Give the extent of all Plasmodium ovale-infected red blood cells.
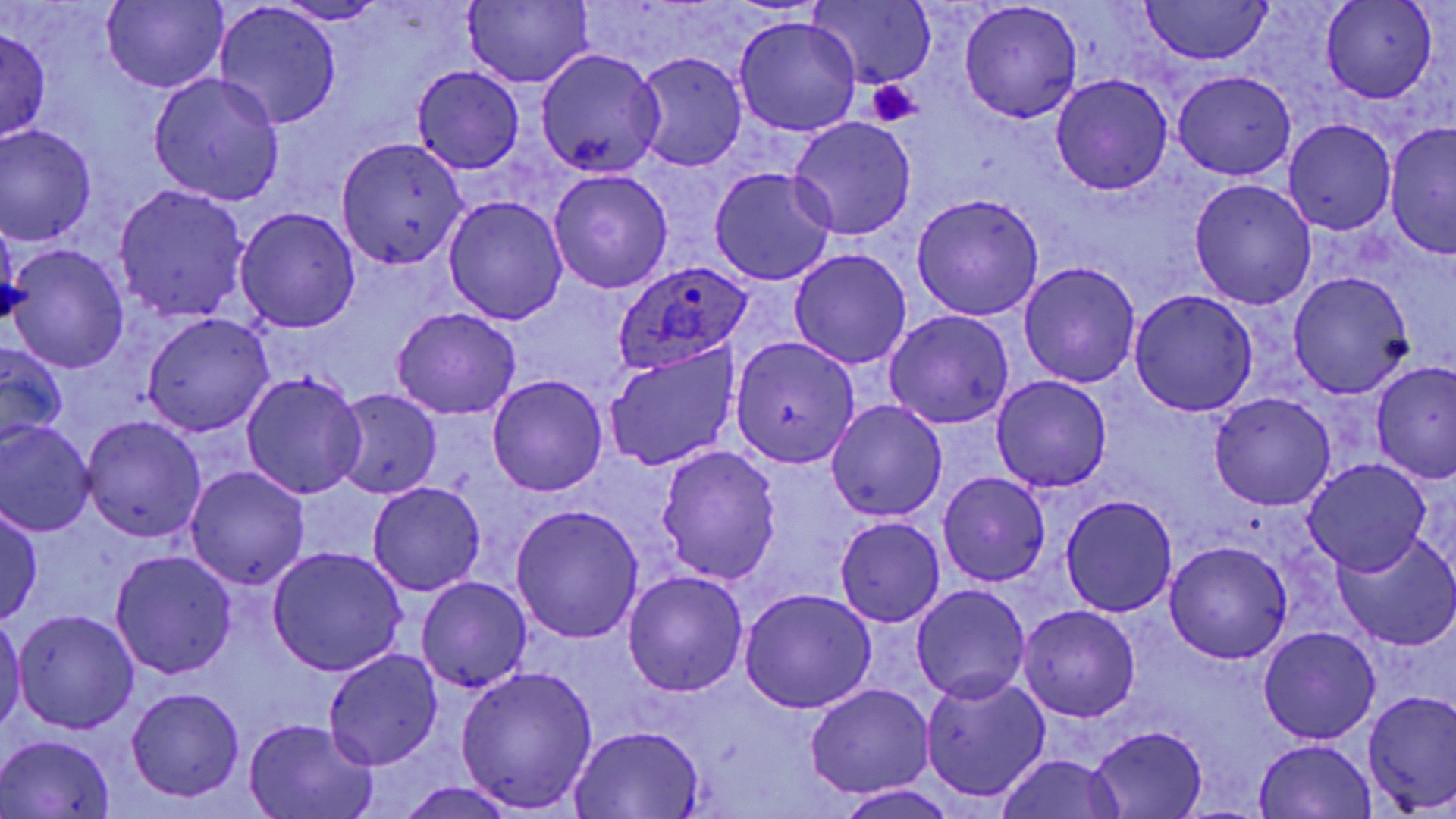
Approximate bounding boxes as [x1, y1, x2, y2] in pixels.
Plasmodium ovale-infected red blood cells: [613, 260, 755, 373].

Platelet locations: [866, 78, 924, 126]. Uninfected red blood cell locations: [805, 0, 936, 90], [1321, 0, 1437, 103], [102, 2, 227, 92], [278, 2, 390, 24], [463, 2, 593, 87], [1138, 2, 1273, 64], [216, 3, 342, 130], [959, 3, 1083, 122], [733, 15, 862, 138], [0, 29, 51, 142], [535, 48, 665, 176], [632, 51, 748, 173], [413, 65, 524, 173], [1173, 69, 1295, 178], [148, 72, 285, 205], [1051, 73, 1173, 195], [788, 117, 917, 241], [1283, 119, 1396, 235], [1385, 122, 1456, 256], [0, 125, 96, 245], [336, 136, 468, 268], [708, 166, 836, 287], [547, 170, 674, 294], [1188, 179, 1317, 309], [114, 185, 250, 324], [912, 193, 1045, 322], [443, 195, 568, 325], [234, 207, 361, 334], [0, 213, 25, 332], [4, 243, 129, 372], [789, 248, 912, 369], [1018, 261, 1141, 388], [1287, 271, 1414, 399], [1129, 289, 1259, 414], [391, 307, 521, 420], [884, 309, 1015, 430], [142, 313, 274, 436], [732, 335, 860, 468], [0, 340, 68, 449], [603, 344, 740, 471], [1371, 360, 1455, 486], [241, 371, 366, 499], [489, 375, 607, 495], [991, 375, 1112, 494], [332, 390, 442, 500], [1210, 392, 1335, 510], [825, 399, 948, 522], [80, 415, 208, 543], [0, 420, 96, 536], [655, 445, 782, 586], [1303, 459, 1432, 577], [186, 465, 310, 591], [937, 471, 1051, 587], [368, 481, 486, 596], [1061, 494, 1178, 616], [0, 504, 44, 624], [510, 504, 643, 641], [311, 507, 461, 640], [834, 515, 946, 627], [1053, 529, 1171, 684], [1331, 530, 1456, 652], [1164, 539, 1293, 663], [267, 547, 407, 676], [109, 552, 237, 678], [622, 571, 748, 697], [416, 577, 531, 693], [911, 584, 1032, 705], [739, 590, 877, 713], [1019, 605, 1141, 722], [13, 609, 140, 734], [0, 615, 27, 736], [1259, 628, 1379, 745], [323, 649, 444, 770], [454, 665, 599, 813], [921, 674, 1050, 802], [804, 684, 935, 799], [126, 687, 244, 800], [1361, 689, 1456, 815], [244, 718, 380, 818], [570, 725, 704, 816], [1090, 726, 1208, 817], [2, 734, 116, 816], [1253, 738, 1378, 818], [994, 753, 1126, 819], [395, 779, 520, 819], [833, 783, 959, 818]. Slide-level diagnosis: Plasmodium ovale. 1000x magnification. Thin blood smear. One field of a larger specimen. May-Grünwald-Giemsa-stained preparation. Image is 1456×819 pixels. Light microscopy.